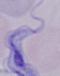
1000x magnification. A trypanosome is seen. Photomicrograph.